Assess for malaria.
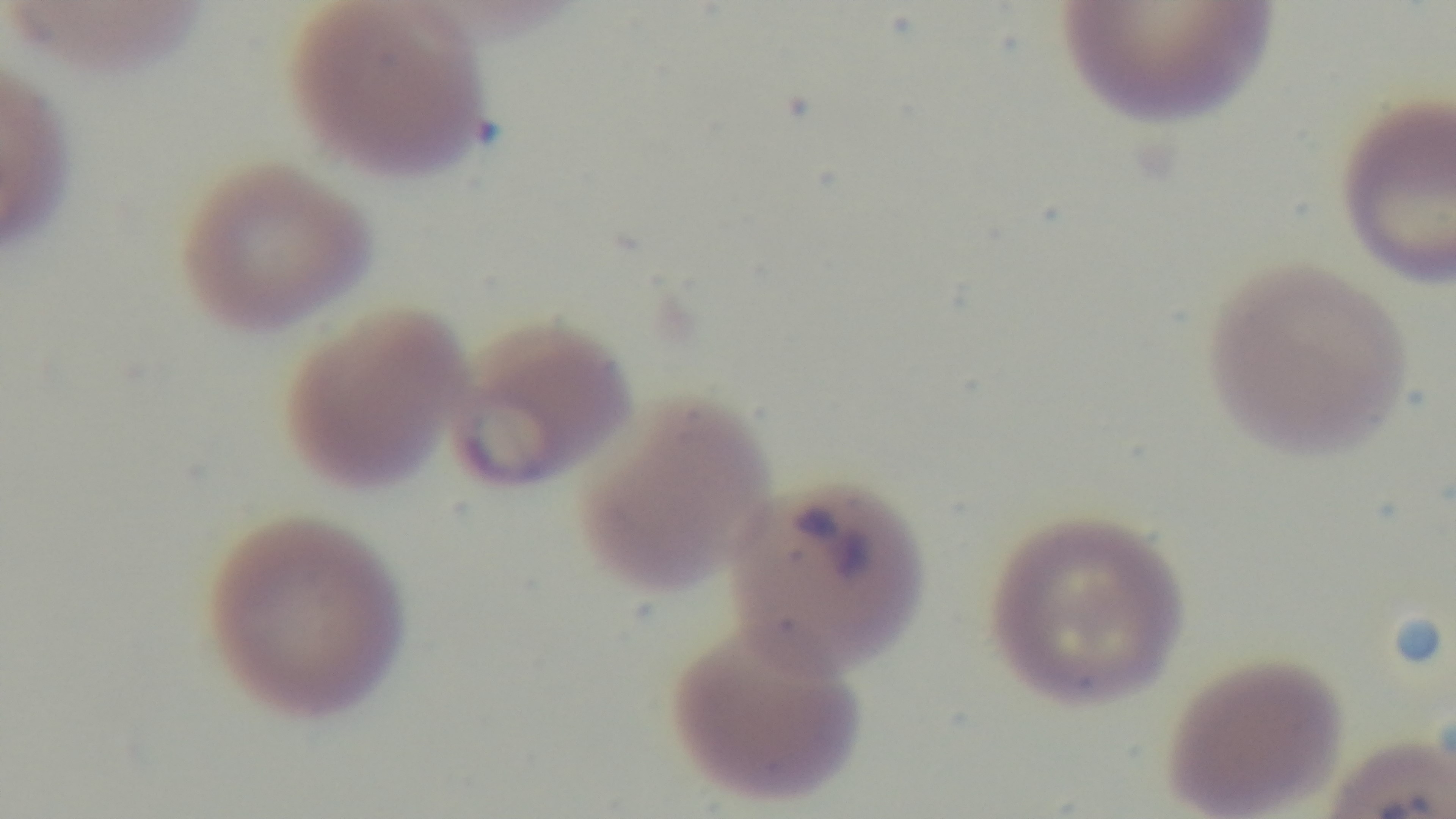
It is infected.

stain = Giemsa
modality = light microscopy
field of view = single
objective = 100x oil immersion
capture = mounted 4K digital camera
preparation = thin